Name the parasite shown.
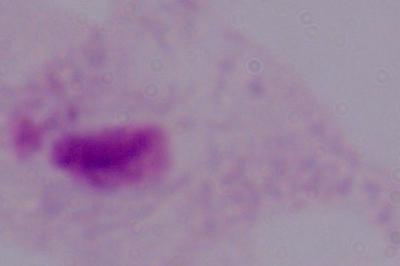
A trichomonad.

Summary:
  - Modality: photomicrograph
  - Magnification: 1000x